Identify the blood parasite species.
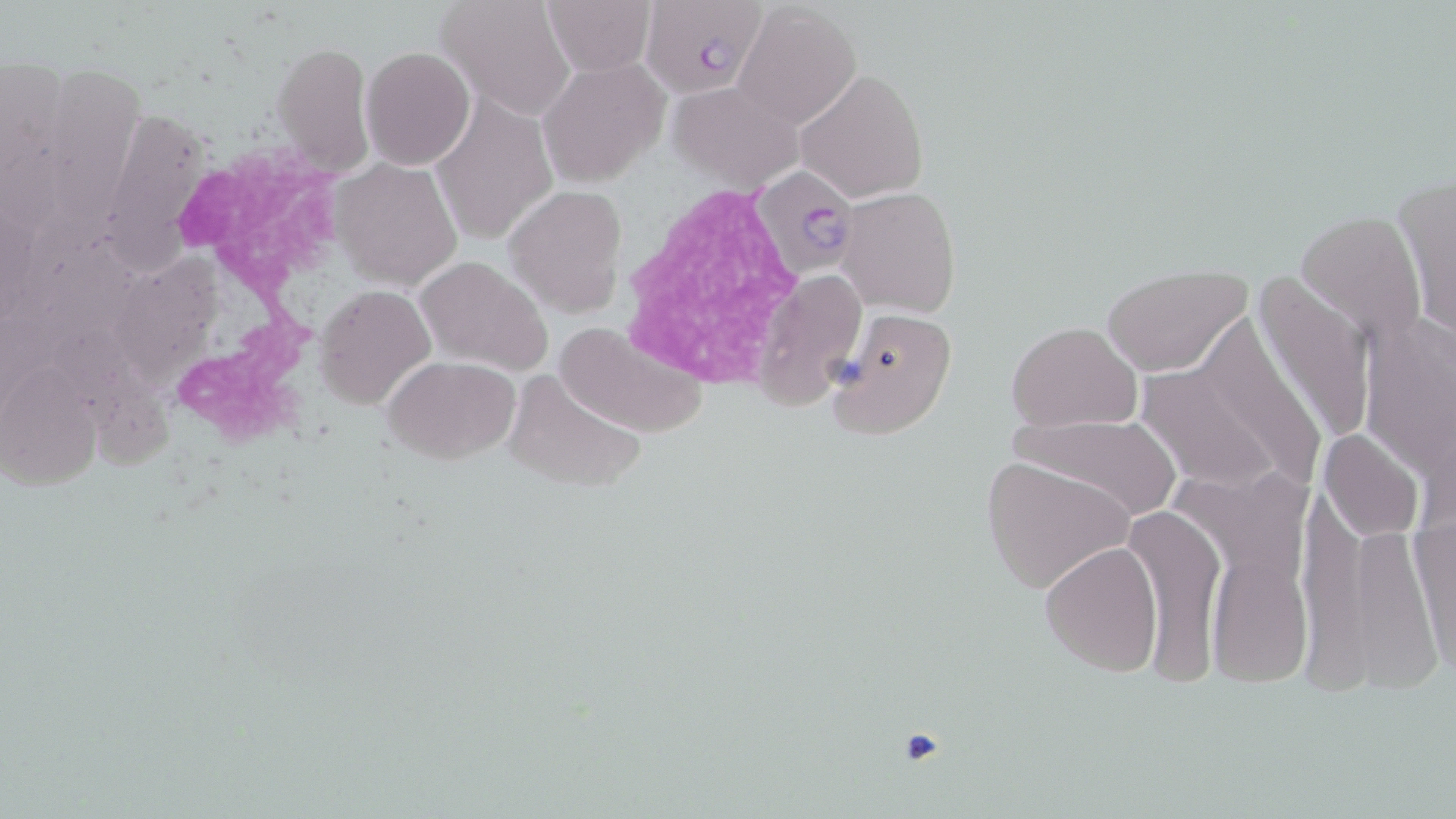

Plasmodium falciparum.

Summary:
  - Coordinate format: approximate bounding boxes as named x1/y1/x2/y2 corners in pixels
  - Plasmodium falciparum-infected red blood cell locations: (x1=640, y1=3, x2=767, y2=100), (x1=753, y1=163, x2=858, y2=279)
  - Platelet locations: (x1=892, y1=725, x2=954, y2=774)
  - White blood cell locations: (x1=165, y1=137, x2=359, y2=462), (x1=616, y1=185, x2=805, y2=388)
  - Uninfected red blood cell locations: (x1=436, y1=0, x2=576, y2=120), (x1=540, y1=0, x2=655, y2=73), (x1=731, y1=3, x2=861, y2=130), (x1=272, y1=40, x2=374, y2=178), (x1=0, y1=43, x2=78, y2=245), (x1=361, y1=46, x2=476, y2=170), (x1=54, y1=58, x2=151, y2=236), (x1=538, y1=58, x2=665, y2=186), (x1=795, y1=69, x2=927, y2=202), (x1=667, y1=80, x2=805, y2=193), (x1=432, y1=93, x2=557, y2=246), (x1=117, y1=111, x2=213, y2=279), (x1=330, y1=156, x2=463, y2=290), (x1=1393, y1=171, x2=1456, y2=347), (x1=506, y1=184, x2=628, y2=320), (x1=836, y1=187, x2=960, y2=317), (x1=1295, y1=207, x2=1426, y2=345), (x1=416, y1=255, x2=550, y2=375), (x1=117, y1=259, x2=221, y2=387), (x1=1101, y1=266, x2=1251, y2=376), (x1=1245, y1=269, x2=1376, y2=455), (x1=750, y1=271, x2=867, y2=410), (x1=316, y1=285, x2=434, y2=408), (x1=826, y1=307, x2=958, y2=440), (x1=44, y1=311, x2=180, y2=485), (x1=1359, y1=314, x2=1453, y2=485), (x1=555, y1=320, x2=709, y2=439), (x1=1006, y1=321, x2=1142, y2=431), (x1=1135, y1=352, x2=1305, y2=498), (x1=382, y1=354, x2=520, y2=463), (x1=1, y1=365, x2=99, y2=490), (x1=505, y1=369, x2=645, y2=494), (x1=1007, y1=411, x2=1182, y2=520), (x1=1318, y1=426, x2=1427, y2=542), (x1=981, y1=455, x2=1133, y2=596), (x1=1129, y1=504, x2=1224, y2=687), (x1=1412, y1=517, x2=1456, y2=678), (x1=1039, y1=541, x2=1163, y2=674), (x1=1209, y1=553, x2=1312, y2=686)
  - Stain: May-Grünwald-Giemsa
  - Field of view: single
  - Magnification: 1000x
  - Modality: light microscopy
  - Image size: 1456×819 pixels
  - Preparation: thin blood film